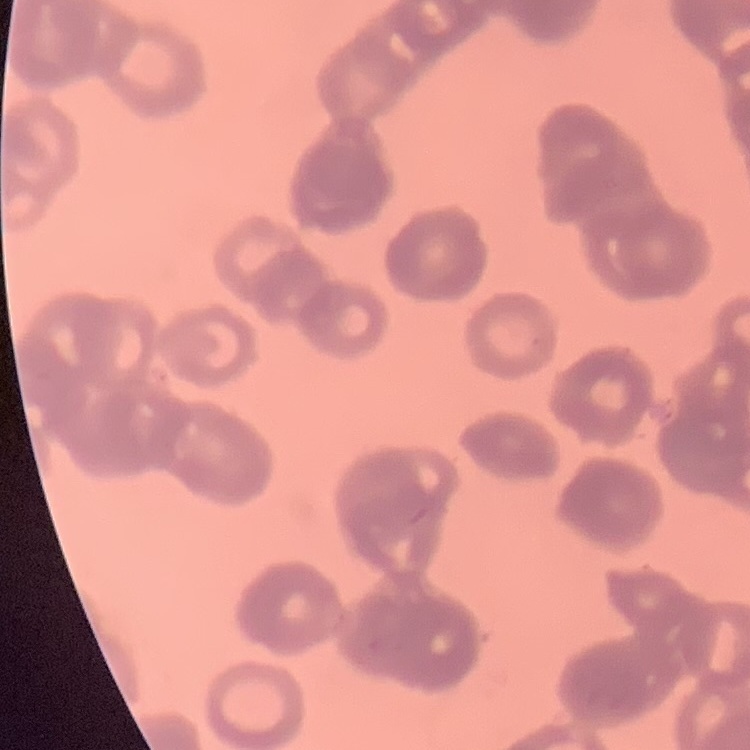
Summary:
  - Red blood cell morphology: rouleaux formation
  - Stain: Field's or Giemsa
  - Image type: one tile cut from a larger photomicrograph
  - Preparation: thin blood film